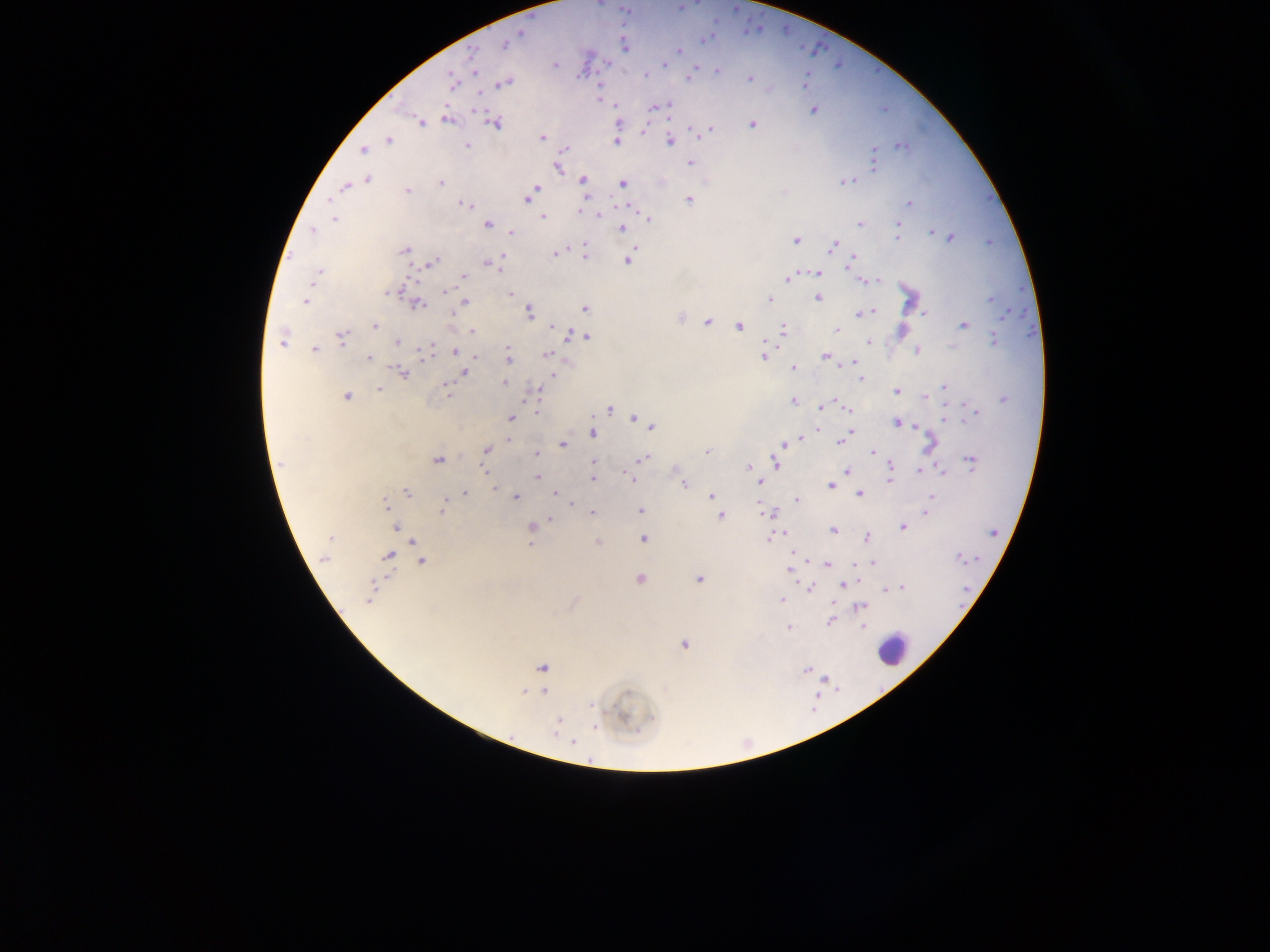

{
  "image_size": "1270×952 pixels",
  "field_of_view": "single",
  "preparation": "thick blood smear",
  "plasmodium_parasite_locations": "approximate centers as [x, y] in pixels: [520, 34], [704, 40], [504, 45], [624, 45], [679, 50], [472, 53], [607, 63], [665, 63], [555, 64], [717, 70], [474, 72], [645, 74], [690, 77], [452, 79], [750, 79], [805, 82], [505, 84], [615, 105], [659, 105], [666, 105], [812, 110], [448, 120], [422, 123], [495, 123], [618, 123], [752, 124], [708, 130], [541, 137], [388, 141], [669, 141], [616, 142], [467, 146], [901, 146], [565, 149], [362, 150], [873, 156], [690, 163], [874, 164], [557, 168], [368, 179], [582, 180], [845, 181], [440, 182], [623, 183], [345, 187], [537, 187], [407, 190], [585, 198], [527, 199], [689, 199], [909, 203], [465, 205], [580, 210], [599, 215], [542, 217], [648, 218], [334, 220], [860, 223], [488, 224], [898, 225], [621, 228], [312, 231], [512, 232], [932, 232], [897, 236], [950, 238], [796, 240], [584, 245], [833, 245], [635, 248], [403, 250], [585, 253], [554, 254], [503, 257], [852, 259], [629, 260], [431, 262], [488, 263], [499, 267], [318, 273], [817, 273], [463, 276], [788, 278], [870, 280], [403, 289], [445, 291], [394, 292], [386, 294], [510, 294], [818, 298], [770, 299], [990, 300], [304, 301], [464, 301], [417, 304], [585, 309], [872, 311], [529, 312], [452, 313], [860, 314], [925, 314], [680, 318], [707, 322], [375, 326], [964, 326], [553, 327], [739, 327], [783, 329], [837, 330], [472, 331], [569, 335], [342, 336], [587, 337], [994, 339], [397, 341], [281, 342], [868, 342], [431, 348], [314, 349], [918, 350], [455, 351], [508, 351], [427, 353], [547, 355], [476, 356], [764, 356], [824, 356], [369, 357], [508, 357], [854, 362], [794, 367], [464, 371], [403, 372], [554, 374], [861, 379], [504, 383], [944, 387], [378, 388], [447, 389], [538, 391], [896, 391], [347, 396], [925, 396], [1003, 398], [793, 400], [820, 407], [845, 408], [610, 410], [974, 412], [634, 417], [510, 418], [944, 419], [897, 423], [916, 426], [651, 427], [817, 429], [592, 433], [798, 439], [509, 441], [839, 442], [563, 444], [784, 444], [929, 445], [487, 450], [707, 451], [872, 452], [536, 453], [643, 459], [437, 460], [594, 462], [775, 462], [971, 462], [891, 465], [749, 467], [677, 470], [920, 470], [847, 471], [942, 473], [537, 477], [753, 477], [593, 479], [632, 479], [888, 480], [760, 482], [684, 483], [831, 485], [494, 488], [407, 493], [465, 493], [556, 494], [860, 495], [712, 496], [516, 497], [933, 497], [796, 499], [385, 504], [571, 504], [441, 509], [640, 511], [770, 512], [926, 512], [593, 513], [720, 515], [551, 519], [396, 526], [531, 526], [902, 527], [833, 530], [778, 535], [330, 538], [770, 538], [867, 538], [644, 539], [598, 542], [530, 544], [792, 552], [388, 555], [959, 557], [323, 558], [421, 562], [872, 562], [827, 563], [857, 564], [789, 571], [639, 578], [699, 579], [845, 583], [899, 587], [811, 588], [886, 588], [368, 600], [781, 601], [860, 607], [830, 622], [862, 626], [788, 628], [684, 644], [542, 667], [806, 669], [542, 691], [525, 692], [627, 692], [590, 706], [557, 725], [596, 727], [573, 743]",
  "capture": "mobile-phone photograph through a microscope",
  "leukocyte_locations": "approximate centers as [x, y] in pixels: [908, 297], [902, 330], [893, 650]",
  "country": "Ghana"
}